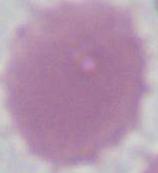

modality = photomicrograph
identification = erythrocyte
magnification = 1000x